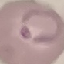
result: malaria parasites identified
capture: smartphone through the microscope eyepiece
preparation: thin blood smear
image_type: cell patch, automatically extracted from a larger field of view and resized to 64 × 64 pixels
stain: Giemsa